Report the malaria status of this cell.
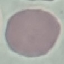
It is uninfected.

Summary:
  - Stain: Giemsa
  - Preparation: thin blood smear
  - Image type: automatically extracted cell patch, resized to 64 × 64 pixels
  - Capture: smartphone through the microscope eyepiece